Outline each blood parasite and name the species.
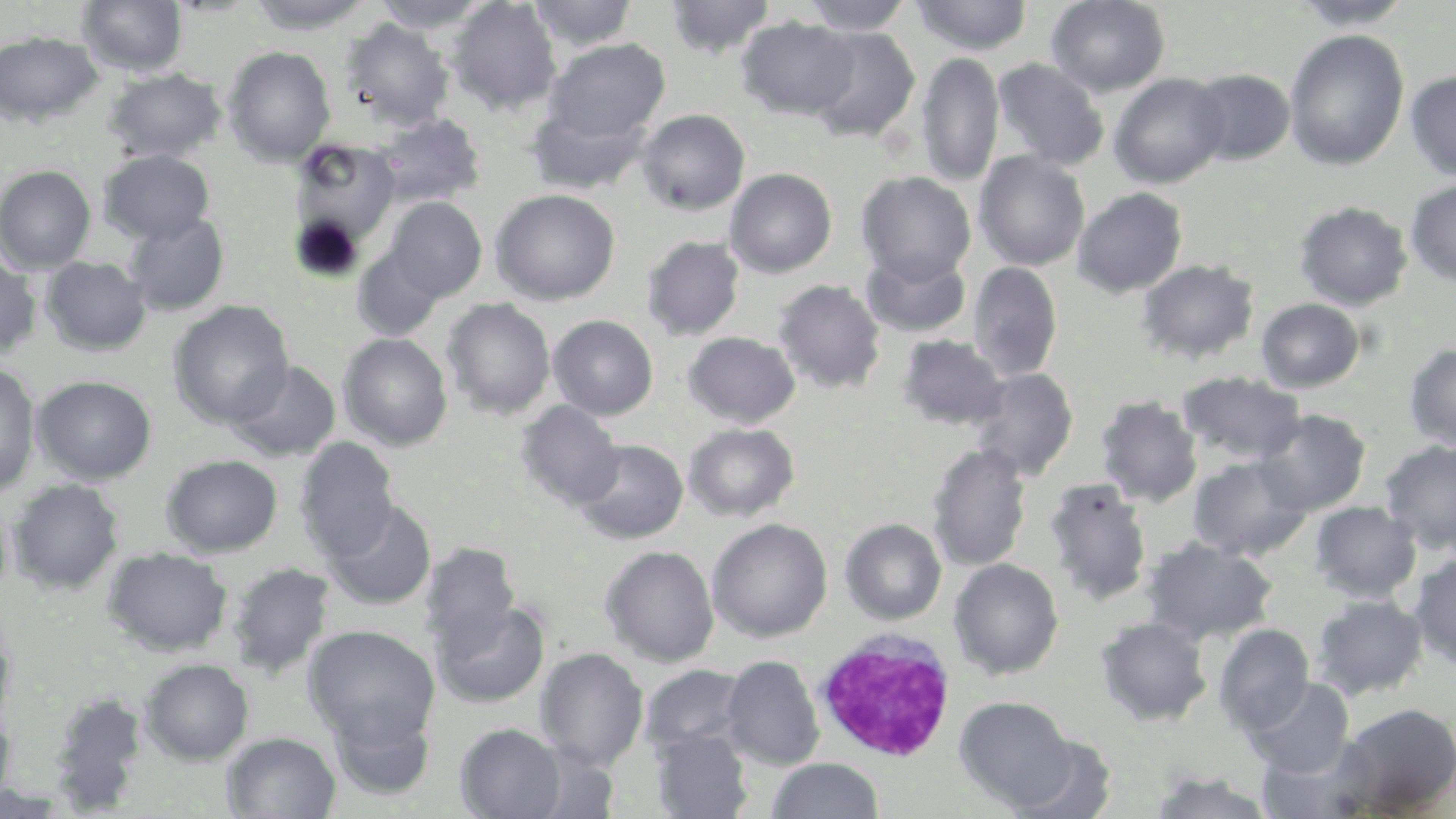
No blood parasites observed.

slide-level diagnosis = no evidence of blood parasites
magnification = 1000x
image size = 1456×819 pixels
uninfected red blood cell locations = approximate bounding boxes as named x1/y1/x2/y2 corners in pixels: (x1=77, y1=0, x2=187, y2=76), (x1=248, y1=0, x2=373, y2=34), (x1=372, y1=0, x2=491, y2=34), (x1=447, y1=0, x2=562, y2=115), (x1=665, y1=0, x2=776, y2=59), (x1=799, y1=0, x2=915, y2=35), (x1=910, y1=0, x2=1033, y2=56), (x1=1046, y1=0, x2=1169, y2=96), (x1=1289, y1=0, x2=1415, y2=30), (x1=527, y1=1, x2=639, y2=51), (x1=736, y1=16, x2=858, y2=119), (x1=341, y1=18, x2=454, y2=131), (x1=804, y1=25, x2=921, y2=142), (x1=1284, y1=28, x2=1409, y2=170), (x1=0, y1=31, x2=103, y2=127), (x1=543, y1=38, x2=670, y2=145), (x1=222, y1=46, x2=336, y2=164), (x1=916, y1=51, x2=1005, y2=186), (x1=992, y1=58, x2=1110, y2=171), (x1=104, y1=69, x2=226, y2=162), (x1=1188, y1=69, x2=1295, y2=165), (x1=1405, y1=69, x2=1456, y2=182), (x1=1108, y1=73, x2=1230, y2=189), (x1=527, y1=100, x2=651, y2=196), (x1=637, y1=109, x2=750, y2=215), (x1=641, y1=111, x2=746, y2=338), (x1=375, y1=113, x2=485, y2=208), (x1=288, y1=138, x2=404, y2=259), (x1=98, y1=149, x2=215, y2=244), (x1=974, y1=151, x2=1090, y2=271), (x1=0, y1=164, x2=96, y2=273), (x1=724, y1=167, x2=838, y2=278), (x1=856, y1=171, x2=976, y2=285), (x1=1404, y1=180, x2=1456, y2=287), (x1=1072, y1=187, x2=1188, y2=297), (x1=490, y1=189, x2=620, y2=305), (x1=384, y1=197, x2=487, y2=302), (x1=1294, y1=201, x2=1413, y2=310), (x1=123, y1=211, x2=230, y2=316), (x1=642, y1=236, x2=745, y2=340), (x1=352, y1=245, x2=447, y2=340), (x1=861, y1=247, x2=972, y2=338), (x1=0, y1=252, x2=41, y2=360), (x1=40, y1=256, x2=151, y2=356), (x1=1137, y1=259, x2=1259, y2=365), (x1=967, y1=261, x2=1063, y2=381), (x1=773, y1=279, x2=886, y2=395), (x1=442, y1=298, x2=556, y2=419), (x1=1256, y1=298, x2=1365, y2=392), (x1=168, y1=300, x2=294, y2=429), (x1=548, y1=315, x2=658, y2=420), (x1=683, y1=331, x2=800, y2=429), (x1=338, y1=333, x2=453, y2=450), (x1=897, y1=334, x2=1008, y2=431), (x1=1403, y1=342, x2=1456, y2=450), (x1=228, y1=360, x2=341, y2=461), (x1=0, y1=362, x2=42, y2=499), (x1=968, y1=367, x2=1078, y2=481), (x1=1177, y1=370, x2=1306, y2=465), (x1=32, y1=375, x2=157, y2=485), (x1=1096, y1=396, x2=1203, y2=507), (x1=515, y1=400, x2=625, y2=510), (x1=1255, y1=408, x2=1372, y2=515), (x1=683, y1=423, x2=799, y2=522), (x1=295, y1=437, x2=400, y2=561), (x1=574, y1=439, x2=688, y2=544), (x1=1379, y1=439, x2=1456, y2=554), (x1=927, y1=443, x2=1032, y2=572), (x1=161, y1=454, x2=283, y2=557), (x1=1187, y1=454, x2=1313, y2=561), (x1=8, y1=478, x2=124, y2=594), (x1=1043, y1=478, x2=1153, y2=606), (x1=323, y1=500, x2=438, y2=611), (x1=1310, y1=500, x2=1421, y2=603), (x1=707, y1=518, x2=832, y2=642), (x1=840, y1=518, x2=947, y2=624), (x1=1141, y1=538, x2=1278, y2=645), (x1=420, y1=543, x2=520, y2=651), (x1=600, y1=544, x2=719, y2=667), (x1=103, y1=547, x2=231, y2=656), (x1=1407, y1=554, x2=1456, y2=668), (x1=949, y1=559, x2=1064, y2=680), (x1=226, y1=562, x2=336, y2=678), (x1=1311, y1=594, x2=1428, y2=701), (x1=432, y1=600, x2=550, y2=708), (x1=0, y1=615, x2=16, y2=728), (x1=1095, y1=617, x2=1212, y2=726), (x1=303, y1=624, x2=440, y2=747), (x1=1213, y1=624, x2=1314, y2=735), (x1=535, y1=647, x2=648, y2=771), (x1=722, y1=655, x2=824, y2=769), (x1=140, y1=658, x2=254, y2=765), (x1=640, y1=664, x2=748, y2=758), (x1=1245, y1=677, x2=1354, y2=778), (x1=49, y1=691, x2=148, y2=812), (x1=955, y1=697, x2=1075, y2=810), (x1=328, y1=702, x2=436, y2=802), (x1=1333, y1=702, x2=1456, y2=817), (x1=0, y1=707, x2=16, y2=808), (x1=455, y1=723, x2=567, y2=818), (x1=651, y1=728, x2=753, y2=818), (x1=221, y1=732, x2=341, y2=818), (x1=1009, y1=735, x2=1116, y2=819), (x1=1259, y1=739, x2=1371, y2=817), (x1=768, y1=758, x2=882, y2=818), (x1=1148, y1=770, x2=1276, y2=819)
stain = May-Grünwald-Giemsa
preparation = thin blood smear
field of view = one of a larger specimen
modality = optical microscopy
white blood cell locations = approximate bounding boxes as named x1/y1/x2/y2 corners in pixels: (x1=812, y1=627, x2=958, y2=762)